Locate and identify every blood parasite.
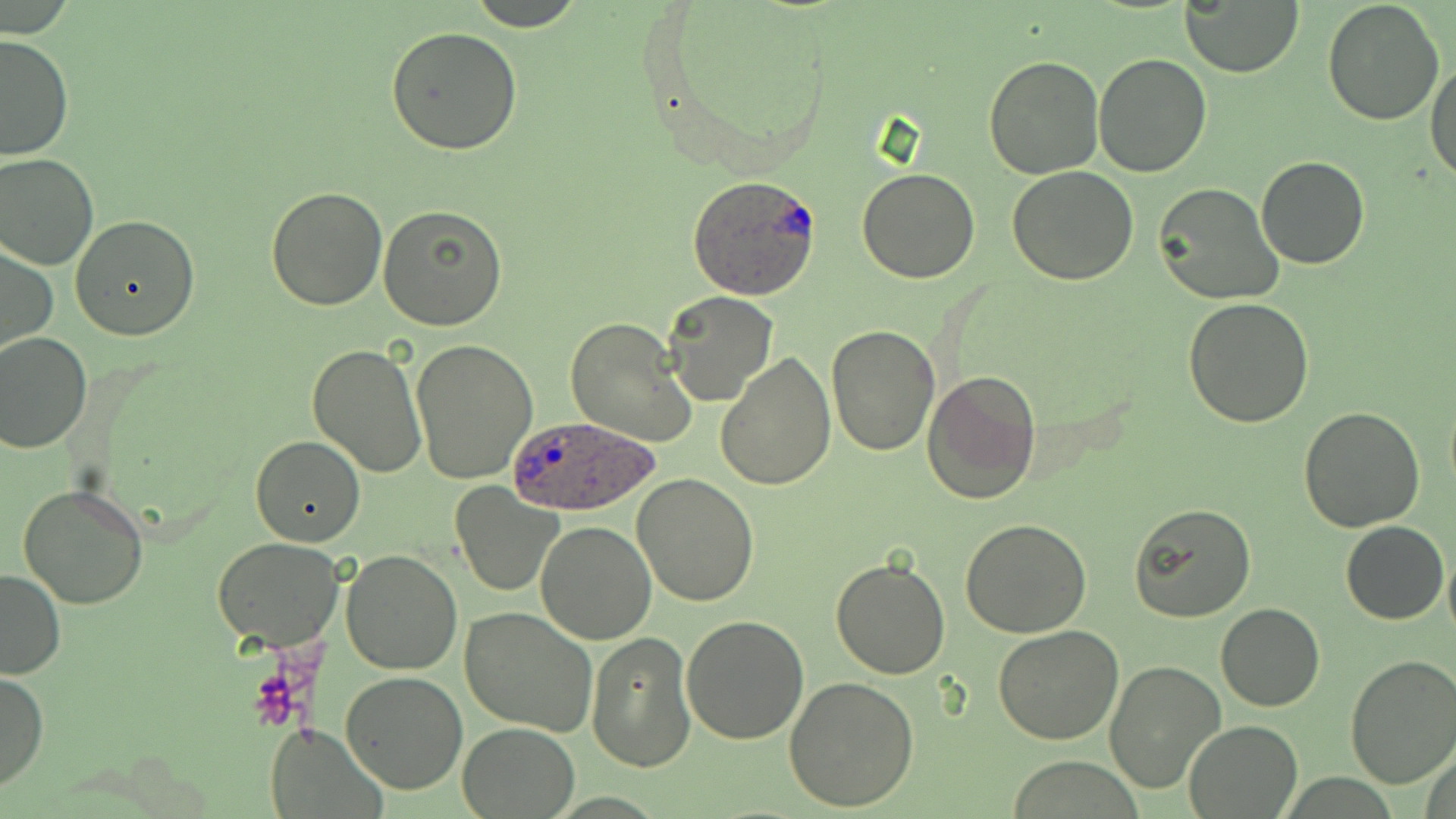
Approximate bounding boxes as (x1, y1, x2, y2) in pixels.
Plasmodium ovale-infected red blood cells: (687, 174, 822, 301), (503, 414, 661, 516).
No Plasmodium falciparum, Plasmodium malariae, Plasmodium vivax, Babesia divergens, or Trypanosoma brucei observed.

Summary:
  - Uninfected red blood cell locations: (466, 0, 587, 29), (1183, 1, 1302, 77), (1321, 1, 1444, 125), (385, 26, 523, 155), (0, 33, 74, 161), (1093, 52, 1212, 177), (983, 56, 1103, 178), (1428, 61, 1456, 190), (0, 153, 98, 270), (1256, 156, 1369, 269), (857, 166, 981, 283), (1006, 166, 1139, 285), (1156, 184, 1282, 304), (265, 185, 388, 311), (378, 205, 509, 332), (70, 214, 200, 340), (1, 242, 57, 355), (664, 291, 778, 405), (1184, 299, 1315, 428), (565, 316, 696, 448), (827, 323, 939, 456), (0, 332, 92, 455), (412, 339, 537, 483), (307, 343, 428, 478), (716, 351, 836, 490), (921, 369, 1040, 506), (1298, 408, 1425, 533), (250, 434, 365, 548), (634, 473, 759, 608), (449, 482, 564, 597), (19, 484, 148, 608), (1128, 502, 1257, 622), (961, 519, 1092, 638), (1341, 520, 1449, 624), (535, 521, 655, 645), (211, 537, 344, 648), (1443, 542, 1456, 645), (340, 549, 462, 674), (830, 554, 952, 680), (0, 567, 66, 680), (1215, 602, 1324, 713), (459, 607, 598, 736), (681, 614, 811, 742), (993, 625, 1123, 745), (586, 633, 696, 772), (1344, 654, 1456, 789), (1104, 660, 1226, 796), (0, 670, 48, 794), (340, 671, 469, 795), (782, 675, 919, 812), (1184, 720, 1301, 817), (265, 721, 381, 817), (456, 722, 581, 818)
  - Slide-level diagnosis: Plasmodium ovale
  - Image size: 1456×819 pixels
  - Field of view: one of a larger specimen
  - Stain: May-Grünwald-Giemsa
  - Modality: light microscopy
  - Preparation: thin blood film
  - Magnification: 1000x